State which cell type is depicted.
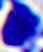

A leukocyte.

Micrograph. 400x magnification.